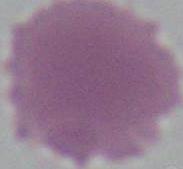
Summary:
  - Modality: micrograph
  - Magnification: 1000x
  - Identification: red blood cell